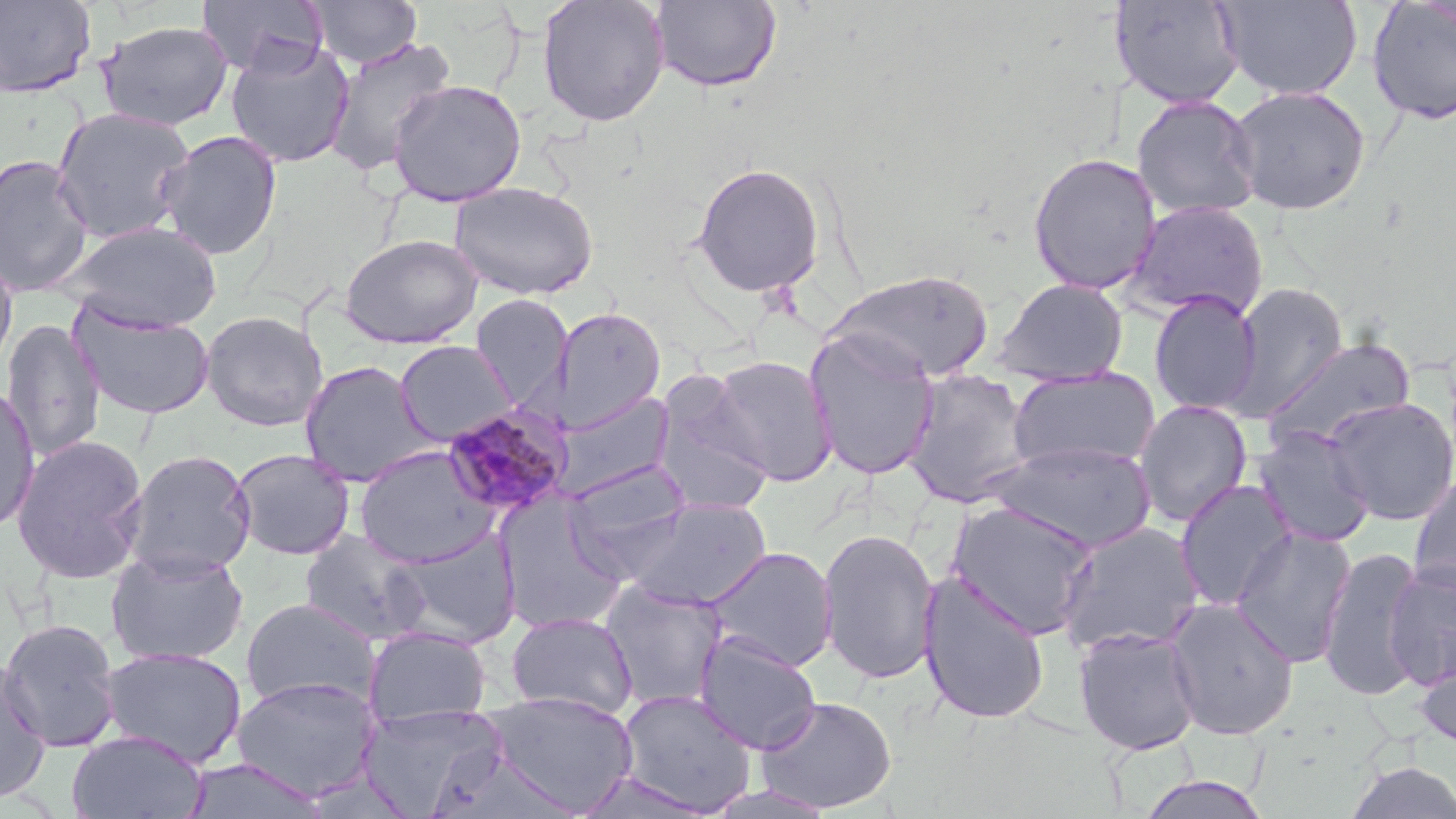

Approximate bounding boxes as [x1, y1, x2, y2] in pixels. Uninfected red blood cell locations: [0, 0, 97, 99], [195, 0, 328, 77], [307, 0, 422, 69], [537, 0, 671, 128], [1216, 0, 1363, 101], [649, 1, 782, 92], [1112, 1, 1245, 110], [1366, 1, 1456, 126], [96, 20, 233, 131], [324, 35, 457, 177], [225, 39, 355, 168], [387, 79, 527, 206], [1227, 84, 1371, 215], [1131, 94, 1262, 222], [50, 107, 196, 244], [156, 130, 283, 261], [1027, 152, 1162, 294], [0, 153, 95, 297], [691, 162, 825, 297], [449, 180, 599, 300], [1125, 200, 1268, 322], [57, 220, 222, 333], [339, 233, 483, 348], [0, 251, 19, 379], [826, 269, 996, 382], [992, 277, 1129, 386], [1225, 283, 1348, 420], [1149, 291, 1262, 416], [469, 293, 573, 408], [71, 305, 215, 420], [555, 306, 667, 432], [199, 310, 328, 432], [1, 319, 107, 461], [804, 329, 940, 480], [1259, 336, 1417, 454], [394, 340, 517, 446], [709, 354, 837, 486], [298, 360, 436, 487], [1006, 367, 1161, 472], [902, 368, 1036, 509], [651, 376, 776, 517], [0, 384, 41, 534], [551, 390, 676, 501], [1323, 396, 1456, 526], [1133, 399, 1253, 528], [1252, 426, 1377, 548], [10, 433, 149, 584], [985, 441, 1158, 552], [353, 445, 500, 568], [229, 448, 355, 561], [122, 449, 257, 579], [563, 459, 693, 569], [1408, 472, 1456, 598], [1174, 478, 1299, 612], [495, 494, 629, 633], [619, 497, 773, 611], [946, 499, 1100, 640], [1054, 520, 1206, 656], [1230, 526, 1357, 667], [817, 527, 941, 685], [299, 528, 429, 646], [387, 530, 522, 648], [702, 546, 838, 673], [1318, 546, 1427, 702], [104, 547, 250, 667], [1384, 564, 1456, 690], [918, 571, 1050, 725], [599, 581, 730, 711], [239, 597, 381, 710], [1165, 597, 1299, 740], [505, 611, 639, 719], [0, 618, 123, 753], [363, 625, 491, 727], [1073, 626, 1204, 755], [693, 631, 821, 754], [1414, 645, 1456, 754], [99, 647, 248, 767], [0, 658, 53, 804], [230, 676, 382, 801], [615, 688, 757, 815], [483, 691, 640, 815], [755, 695, 897, 813], [356, 704, 508, 816], [66, 729, 208, 819], [422, 743, 578, 819], [181, 757, 328, 818], [1344, 760, 1456, 819], [572, 770, 714, 817], [1135, 774, 1273, 818]. Plasmodium malariae-infected red blood cell locations: [440, 403, 574, 519]. Slide-level diagnosis: Plasmodium malariae. One field of a larger specimen. May-Grünwald-Giemsa stain. Image is 1456×819 pixels. Captured at 1000x magnification. Thin blood film. Optical microscopy.